Report the malaria status of this cell.
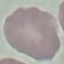

Uninfected.

Giemsa-stained preparation. Thin blood film. Cell patch, automatically extracted from a larger field of view and resized to 64 × 64 pixels. Photographed with a smartphone camera at the microscope eyepiece.